Assess this cell for malaria.
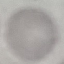
Uninfected.

Summary:
  - Preparation: thin blood smear
  - Capture: smartphone through the microscope eyepiece
  - Stain: Giemsa
  - Image type: automatically extracted cell patch, resized to 64 × 64 pixels